Outline each Babesia divergens-infected red blood cell.
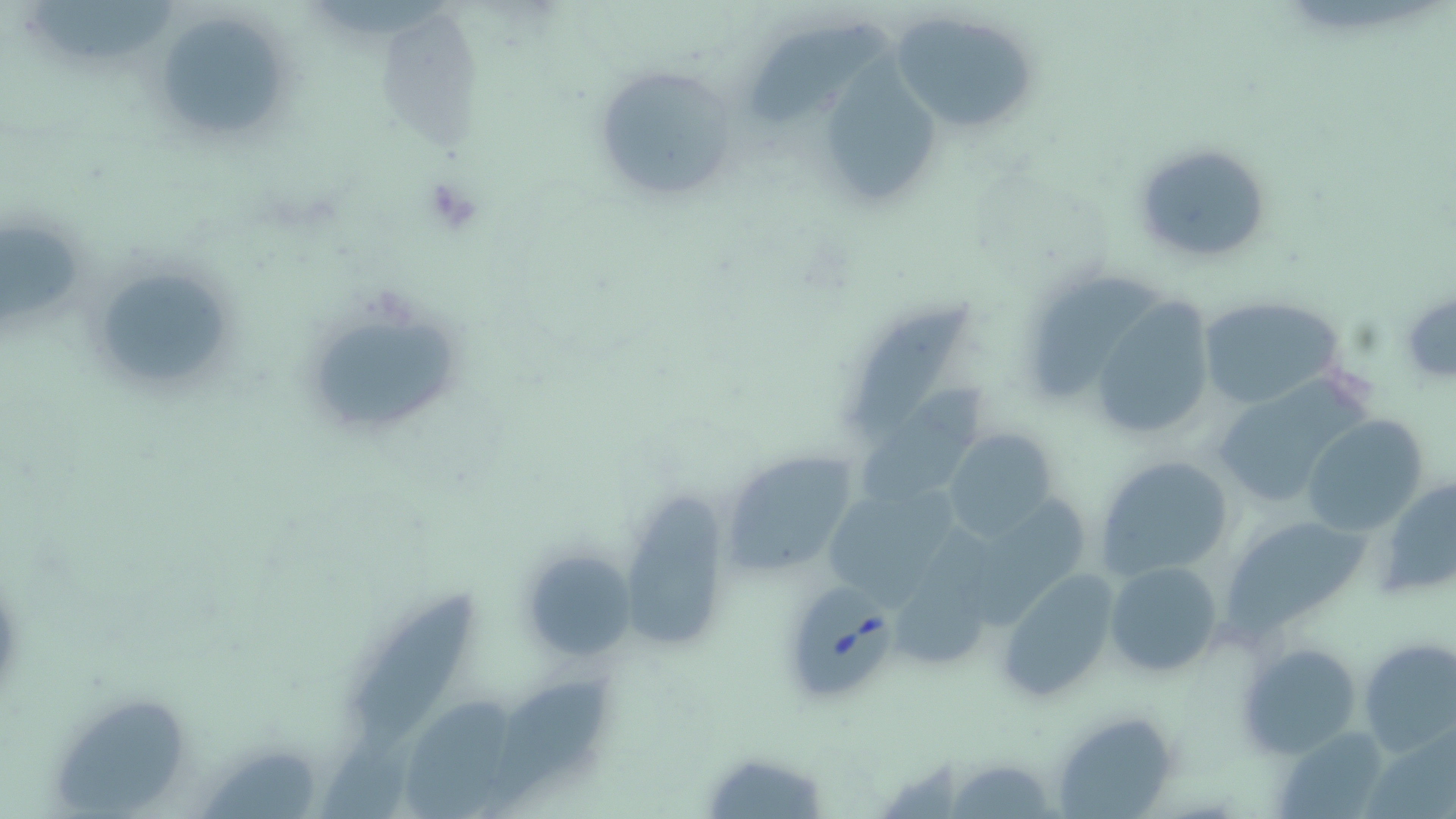

Approximate bounding boxes as named x1/y1/x2/y2 corners in pixels.
Babesia divergens-infected red blood cells: (x1=782, y1=585, x2=896, y2=701).

slide-level diagnosis = Babesia divergens
modality = light microscopy
magnification = 1000x
preparation = thin blood film
image size = 1456×819 pixels
stain = May-Grünwald-Giemsa
field of view = one of a larger specimen
uninfected red blood cell locations = approximate bounding boxes as named x1/y1/x2/y2 corners in pixels: (x1=35, y1=4, x2=181, y2=59), (x1=889, y1=9, x2=1040, y2=134), (x1=748, y1=17, x2=892, y2=127), (x1=162, y1=23, x2=276, y2=129), (x1=824, y1=45, x2=941, y2=202), (x1=591, y1=62, x2=743, y2=202), (x1=1130, y1=137, x2=1275, y2=268), (x1=0, y1=224, x2=82, y2=330), (x1=86, y1=260, x2=242, y2=398), (x1=1028, y1=273, x2=1166, y2=402), (x1=1398, y1=286, x2=1456, y2=386), (x1=1196, y1=296, x2=1346, y2=410), (x1=1090, y1=297, x2=1220, y2=439), (x1=851, y1=302, x2=983, y2=438), (x1=308, y1=311, x2=461, y2=429), (x1=1209, y1=376, x2=1371, y2=512), (x1=862, y1=379, x2=992, y2=505), (x1=1304, y1=416, x2=1430, y2=535), (x1=941, y1=428, x2=1061, y2=543), (x1=719, y1=449, x2=858, y2=577), (x1=1095, y1=456, x2=1238, y2=580), (x1=1381, y1=476, x2=1455, y2=595), (x1=616, y1=488, x2=734, y2=656), (x1=977, y1=488, x2=1086, y2=633), (x1=827, y1=489, x2=960, y2=606), (x1=1223, y1=514, x2=1368, y2=634), (x1=890, y1=525, x2=1009, y2=669), (x1=517, y1=546, x2=633, y2=659), (x1=1105, y1=560, x2=1222, y2=678), (x1=997, y1=568, x2=1122, y2=703), (x1=343, y1=582, x2=477, y2=753), (x1=1359, y1=639, x2=1456, y2=757), (x1=1238, y1=641, x2=1363, y2=760), (x1=485, y1=674, x2=618, y2=819), (x1=394, y1=692, x2=519, y2=819), (x1=60, y1=697, x2=182, y2=816), (x1=1050, y1=710, x2=1180, y2=818), (x1=1274, y1=729, x2=1394, y2=819), (x1=308, y1=739, x2=416, y2=819), (x1=198, y1=749, x2=316, y2=819), (x1=700, y1=749, x2=829, y2=818), (x1=942, y1=755, x2=1060, y2=818)